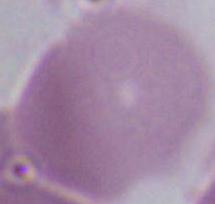
Captured at 1000x magnification. A red blood cell is shown. Micrograph.